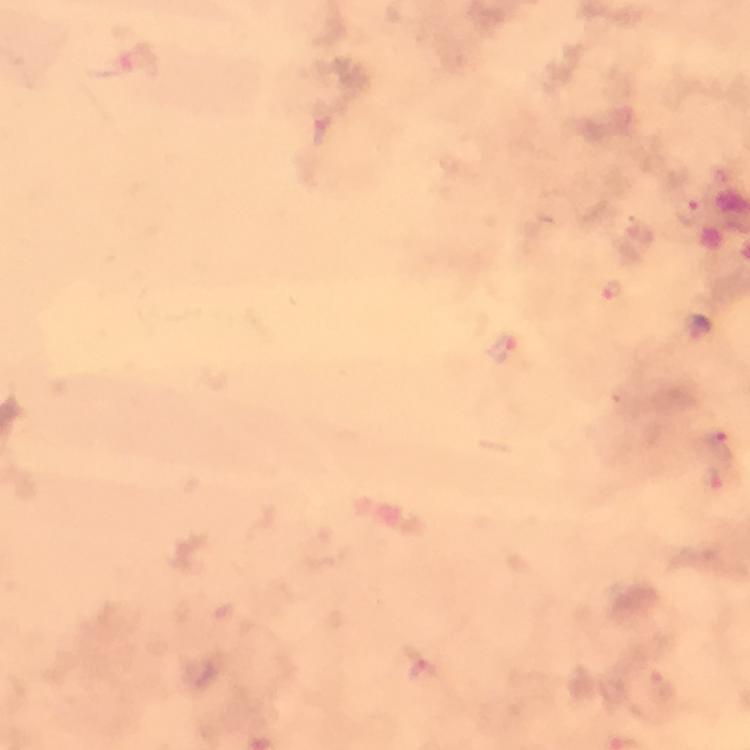
Approximate centers as [x, y] in pixels.
Summary:
  - Plasmodium parasite locations: [690, 210], [613, 292], [502, 350], [720, 444], [716, 480], [423, 673]
  - Cropped from: one field of view
  - Immersion oil: used
  - Stain: Giemsa
  - Preparation: thick smear
  - Capture: smartphone mounted on the microscope
  - Context: from a diagnostic examination for malaria
  - Magnification: 100x
  - Image size: 750×750 pixels